State the preparation type.
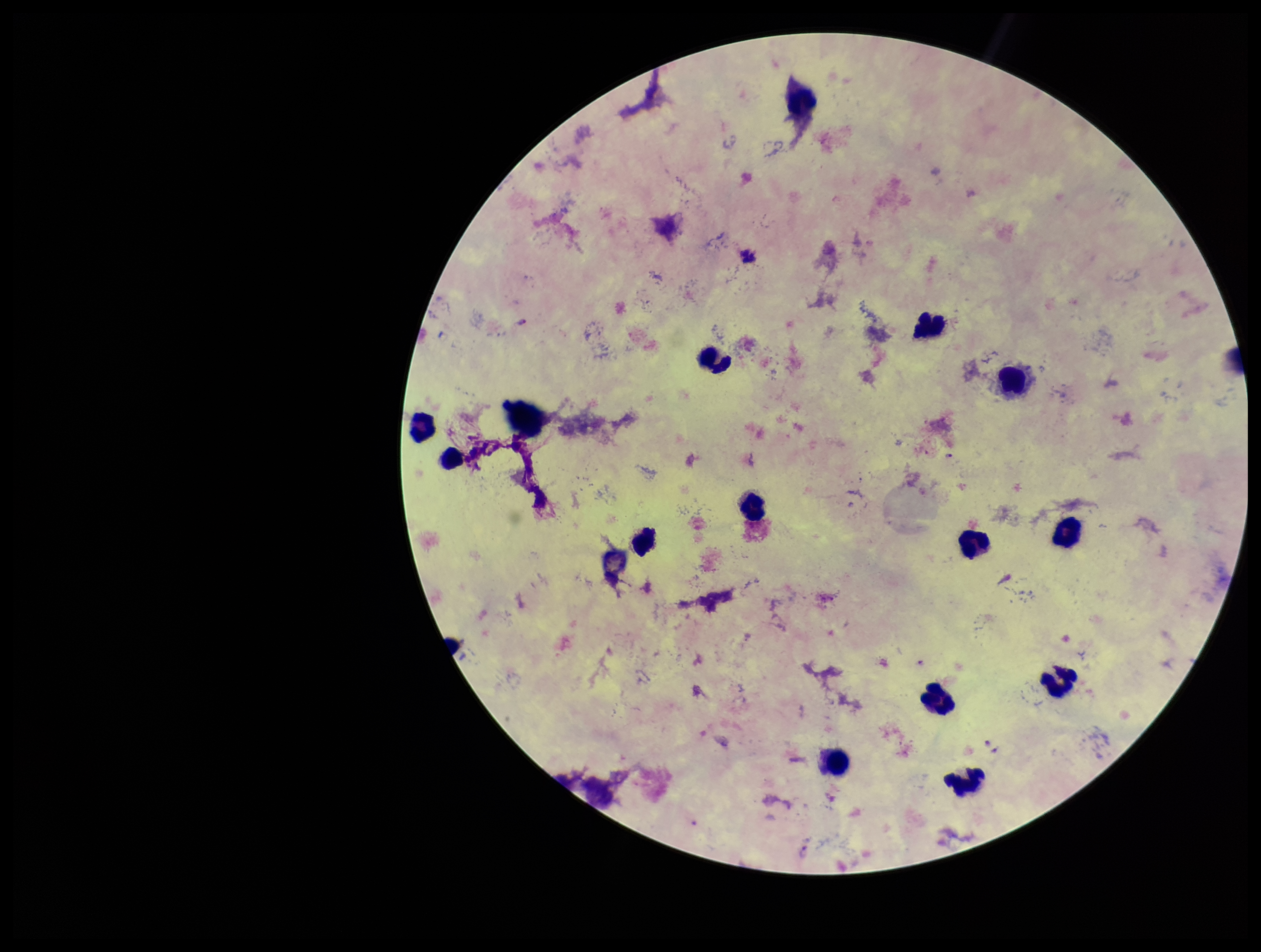
It is a thick blood smear.

Single field of view. Parasite count: 5. Image is 1261×952 pixels. Species reported for this patient: Plasmodium falciparum. Smartphone photograph taken through the eyepiece of a microscope. Stained with Giemsa. Patient malaria status: infected. Leukocyte count: 16. Plasmodium parasites: identified.